Classify this cell by malaria status.
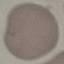

It is uninfected.

capture = smartphone camera at the microscope eyepiece
stain = Giemsa
image type = automatically extracted cell patch, resized to 64 × 64 pixels
preparation = thin blood film